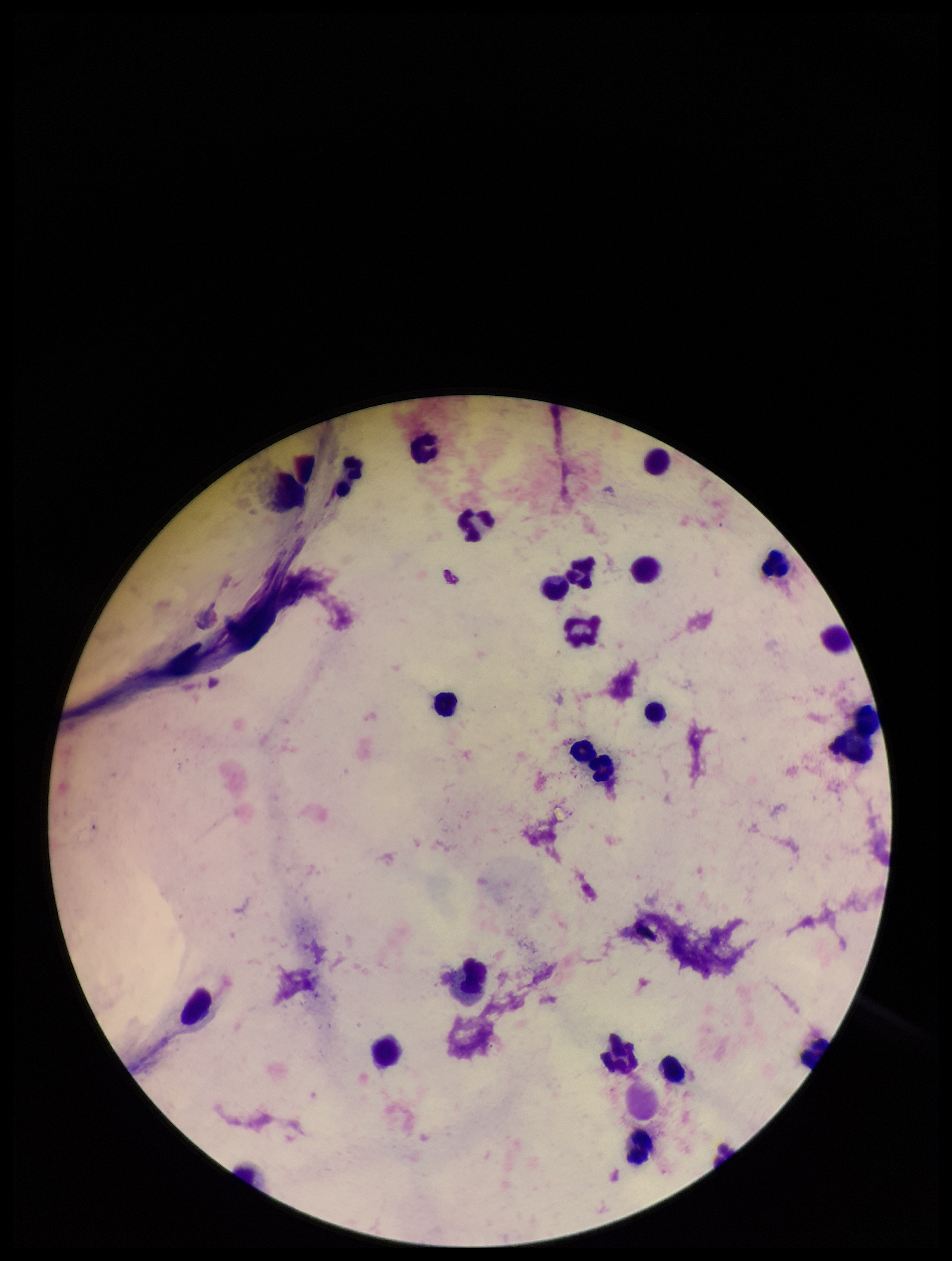
image size = 952×1261 pixels
patient malaria status = negative
leukocyte count = 23
stain = Giemsa
parasite count = 0
Plasmodium parasites = none detected
field of view = single
capture = smartphone photograph through the microscope eyepiece
preparation = thick blood smear